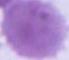

modality = photomicrograph
identification = red blood cell
magnification = 1000x